Report the malaria status of this cell.
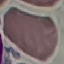
Uninfected.

Photographed with a smartphone camera at the microscope eyepiece. Thin blood film. Giemsa stain. Automatically extracted cell patch, resized to 64 × 64 pixels.